Locate every blood parasite and identify its species.
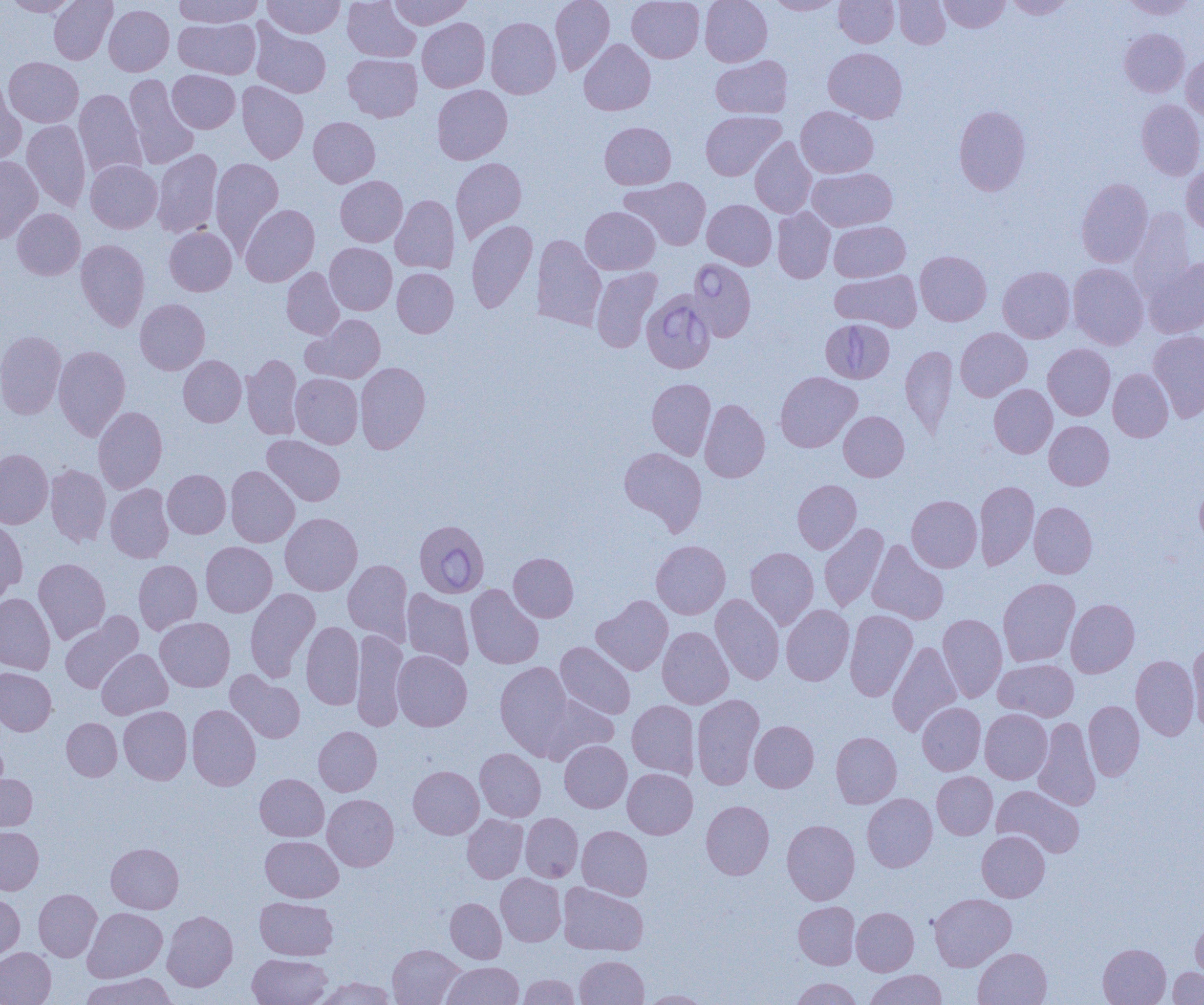

Approximate bounding boxes as [x1, y1, x2, y2] in pixels.
Babesia divergens-infected red blood cells: [687, 258, 756, 342], [641, 290, 716, 374], [820, 318, 894, 383], [413, 518, 489, 599].
No Plasmodium falciparum, Plasmodium ovale, Plasmodium malariae, Plasmodium vivax, or Trypanosoma brucei observed.

slide-level diagnosis = Babesia divergens
image size = 1204×1005 pixels
preparation = thin blood smear
modality = optical microscopy
uninfected red blood cell locations = approximate bounding boxes as [x1, y1, x2, y2] in pixels: [4, 0, 79, 16], [49, 0, 117, 64], [174, 0, 263, 28], [263, 0, 345, 38], [343, 0, 421, 62], [388, 0, 472, 30], [550, 0, 615, 74], [627, 0, 704, 63], [700, 0, 772, 66], [767, 0, 842, 15], [834, 0, 899, 47], [894, 0, 950, 48], [939, 0, 1009, 32], [1005, 0, 1076, 19], [1121, 0, 1198, 19], [104, 4, 174, 76], [486, 17, 561, 98], [174, 18, 261, 79], [417, 18, 490, 92], [250, 23, 331, 98], [1119, 28, 1190, 97], [579, 38, 655, 115], [823, 47, 907, 123], [343, 54, 422, 122], [1181, 54, 1204, 121], [711, 55, 792, 118], [4, 57, 84, 127], [167, 70, 240, 133], [123, 74, 199, 170], [0, 80, 27, 166], [237, 81, 309, 164], [432, 85, 513, 164], [75, 89, 146, 180], [1137, 99, 1204, 180], [953, 105, 1031, 195], [796, 106, 878, 178], [700, 111, 785, 181], [309, 117, 380, 187], [22, 120, 91, 211], [599, 122, 676, 189], [750, 137, 817, 218], [152, 148, 222, 238], [0, 155, 42, 243], [210, 157, 284, 253], [451, 157, 527, 244], [85, 160, 162, 233], [1181, 162, 1204, 235], [808, 168, 897, 231], [335, 176, 408, 246], [620, 177, 711, 251], [1076, 178, 1153, 268], [391, 195, 460, 273], [702, 199, 776, 270], [240, 204, 319, 286], [580, 206, 660, 274], [772, 207, 835, 283], [12, 208, 85, 280], [1128, 208, 1197, 302], [466, 220, 538, 313], [829, 221, 909, 282], [164, 226, 237, 296], [532, 235, 606, 330], [76, 239, 150, 331], [325, 242, 397, 315], [915, 250, 991, 326], [1143, 256, 1204, 338], [1068, 263, 1149, 350], [997, 266, 1075, 343], [281, 267, 344, 339], [591, 267, 661, 352], [392, 268, 458, 337], [831, 270, 922, 332], [135, 299, 210, 374], [303, 314, 386, 383], [955, 327, 1032, 401], [0, 330, 66, 420], [1148, 330, 1204, 422], [1043, 343, 1115, 420], [53, 345, 130, 441], [901, 345, 958, 435], [241, 354, 302, 439], [178, 355, 246, 426], [355, 362, 431, 453], [1108, 368, 1173, 442], [775, 371, 861, 452], [290, 373, 363, 448], [647, 378, 715, 460], [989, 384, 1057, 458], [699, 399, 770, 482], [93, 406, 167, 493], [839, 411, 909, 481], [1044, 421, 1114, 489], [262, 435, 345, 506], [619, 447, 707, 535], [0, 449, 53, 528], [46, 465, 111, 547], [226, 466, 300, 547], [163, 469, 231, 538], [792, 479, 861, 553], [974, 481, 1039, 570], [105, 483, 174, 563], [1195, 483, 1204, 547], [907, 495, 982, 572], [1029, 501, 1097, 578], [280, 512, 362, 595], [0, 519, 27, 602], [819, 523, 889, 612], [867, 539, 948, 625], [651, 540, 730, 619], [201, 541, 277, 616], [746, 547, 819, 629], [509, 552, 579, 622], [33, 558, 111, 644], [134, 559, 202, 634], [343, 559, 413, 645], [997, 577, 1080, 666], [465, 584, 544, 669], [245, 588, 320, 682], [402, 589, 474, 670], [0, 592, 55, 674], [710, 593, 784, 684], [592, 595, 673, 676], [1066, 598, 1139, 677], [781, 604, 854, 685], [845, 609, 917, 701], [60, 612, 142, 694], [938, 613, 1007, 702], [155, 617, 235, 692], [301, 622, 364, 710], [657, 626, 734, 709], [351, 630, 408, 731], [1187, 640, 1204, 732], [887, 641, 962, 737], [555, 642, 635, 719], [97, 649, 172, 719], [392, 650, 472, 731], [1131, 655, 1199, 740], [995, 658, 1079, 721], [495, 661, 574, 755], [0, 667, 57, 735], [226, 671, 305, 743], [533, 693, 618, 764], [691, 694, 764, 789], [627, 700, 700, 778], [1084, 701, 1144, 781], [917, 702, 986, 775], [187, 704, 261, 790], [119, 706, 192, 784], [980, 709, 1052, 784], [1033, 717, 1100, 810], [62, 718, 122, 780], [749, 720, 819, 792], [313, 726, 382, 796], [831, 732, 902, 808], [0, 736, 7, 801], [559, 740, 632, 812], [475, 748, 546, 821], [408, 765, 484, 839], [623, 768, 698, 839], [932, 771, 998, 839], [0, 772, 37, 833], [255, 773, 329, 841], [992, 784, 1084, 857], [862, 793, 937, 871], [322, 794, 399, 871], [701, 800, 774, 879], [521, 813, 583, 882], [462, 814, 528, 883], [782, 819, 860, 904], [0, 826, 43, 894], [577, 826, 653, 900], [977, 831, 1050, 902], [261, 835, 343, 902], [106, 843, 183, 913], [496, 873, 566, 946], [558, 882, 648, 955], [34, 888, 102, 961], [0, 892, 25, 961], [929, 893, 1016, 971], [255, 897, 338, 960], [445, 898, 506, 963], [793, 901, 860, 969], [83, 907, 167, 981], [851, 907, 919, 975], [162, 910, 238, 991], [1191, 914, 1204, 982], [1098, 943, 1171, 1005], [387, 944, 464, 1005], [0, 947, 56, 1005], [973, 948, 1051, 1005], [248, 953, 332, 1005], [575, 955, 649, 1004], [443, 961, 524, 1005], [1167, 967, 1204, 1004], [864, 970, 947, 1005], [79, 973, 177, 1005], [518, 974, 580, 1004], [315, 976, 397, 1005], [790, 977, 862, 1005], [641, 990, 712, 1004]
magnification = 1000x
field of view = one of a larger specimen